State which parasite is depicted.
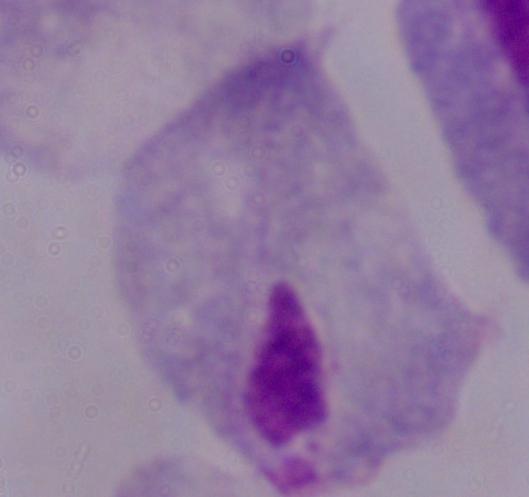
A trichomonad.

Summary:
  - Magnification: 1000x
  - Modality: micrograph